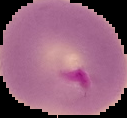

Summary:
  - Preparation: thin blood smear
  - Image type: segmented cell region with the area outside set to black
  - Image size: 127×118 pixels
  - Result: Plasmodium parasites identified